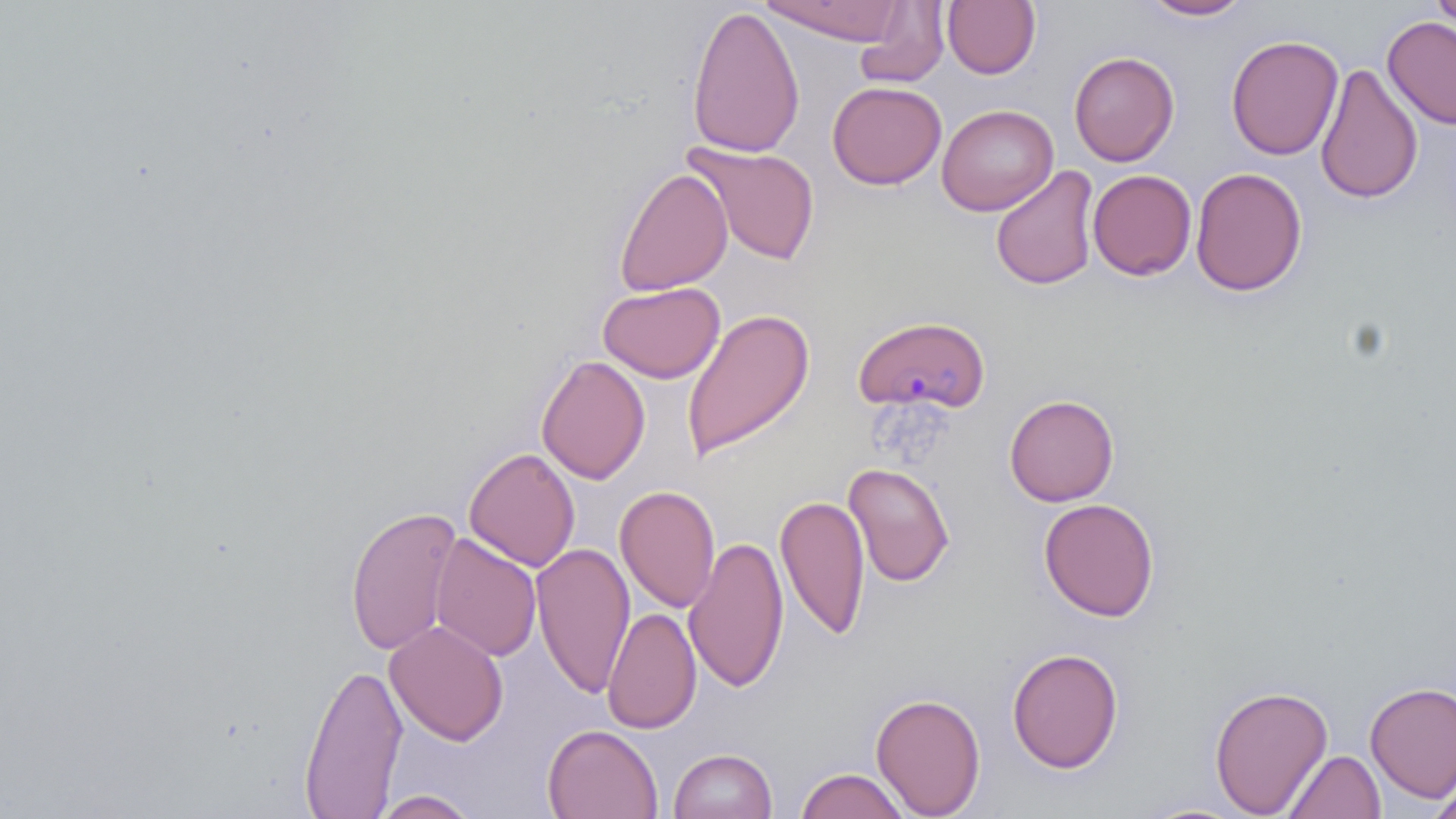
slide_level_diagnosis: Plasmodium malariae
uninfected_red_blood_cell_locations: 'approximate bounding boxes as [x1, y1, x2, y2] in pixels: [762, 0, 909, 44], [1139, 0, 1255, 21], [1428, 0, 1456, 40], [854, 1, 949, 89], [942, 1, 1041, 79], [686, 4, 804, 159], [1382, 15, 1456, 130], [1226, 34, 1344, 161], [1068, 51, 1179, 166], [1314, 63, 1423, 206], [827, 81, 947, 189], [937, 104, 1058, 216], [682, 140, 820, 266], [990, 165, 1100, 291], [614, 167, 733, 296], [1190, 167, 1307, 297], [1087, 169, 1197, 280], [598, 281, 725, 384], [681, 308, 815, 460], [536, 354, 650, 485], [1004, 394, 1119, 506], [464, 447, 580, 572], [843, 461, 955, 587], [615, 485, 720, 614], [775, 494, 871, 640], [1038, 497, 1160, 621], [345, 503, 462, 657], [430, 532, 542, 663], [684, 535, 788, 694], [531, 541, 635, 700], [602, 607, 701, 734], [384, 620, 508, 746], [1007, 646, 1124, 773], [298, 661, 408, 816], [1364, 681, 1456, 802], [1208, 682, 1333, 817], [870, 691, 986, 818], [542, 724, 663, 819], [668, 747, 778, 819], [1284, 749, 1385, 818], [795, 767, 910, 819], [1426, 776, 1456, 819], [371, 790, 480, 818], [1135, 799, 1255, 818]'
field_of_view: one of a larger specimen
stain: May-Grünwald-Giemsa
plasmodium_malariae_infected_red_blood_cell_locations: 'approximate bounding boxes as [x1, y1, x2, y2] in pixels: [853, 313, 991, 414]'
magnification: 1000x
modality: optical microscopy
preparation: thin blood smear
image_size: 1456×819 pixels